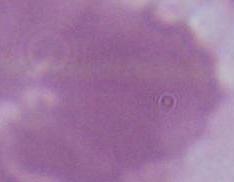

identification = red blood cell
modality = micrograph
magnification = 1000x